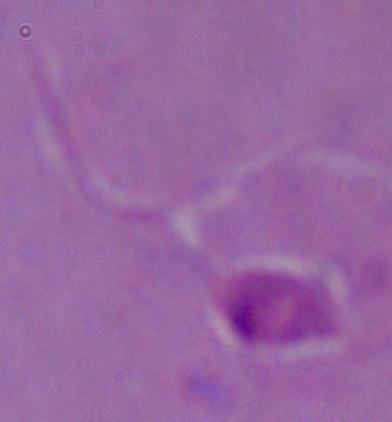

identification = Leishmania
magnification = 1000x
modality = micrograph